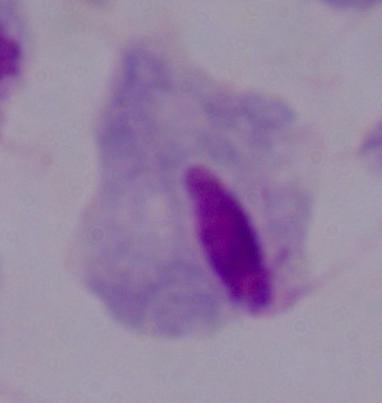
Summary:
  - Modality: photomicrograph
  - Identification: trichomonad
  - Magnification: 1000x